Report the malaria status of this cell.
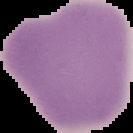
It is uninfected.

image_type: cell region segmented out of the field of view; surrounding area masked to black
image_size: 133×133 pixels
preparation: thin blood film